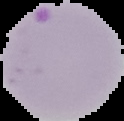

The area outside the segmented cell region is set to black. From a thin blood smear. Image is 124×121 pixels. Malaria status: parasitized.